State which parasite is depicted.
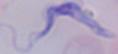
A trypanosome.

Photomicrograph. 1000x magnification.